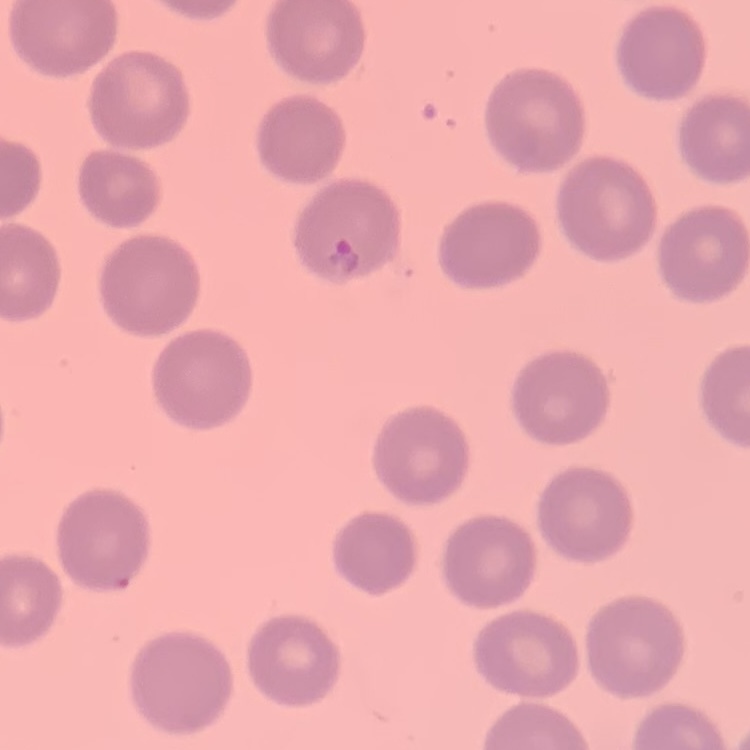

red_blood_cell_morphology: no rouleaux formation
stain: Field's or Giemsa
preparation: thin blood film
image_type: one tile cut from a larger photomicrograph